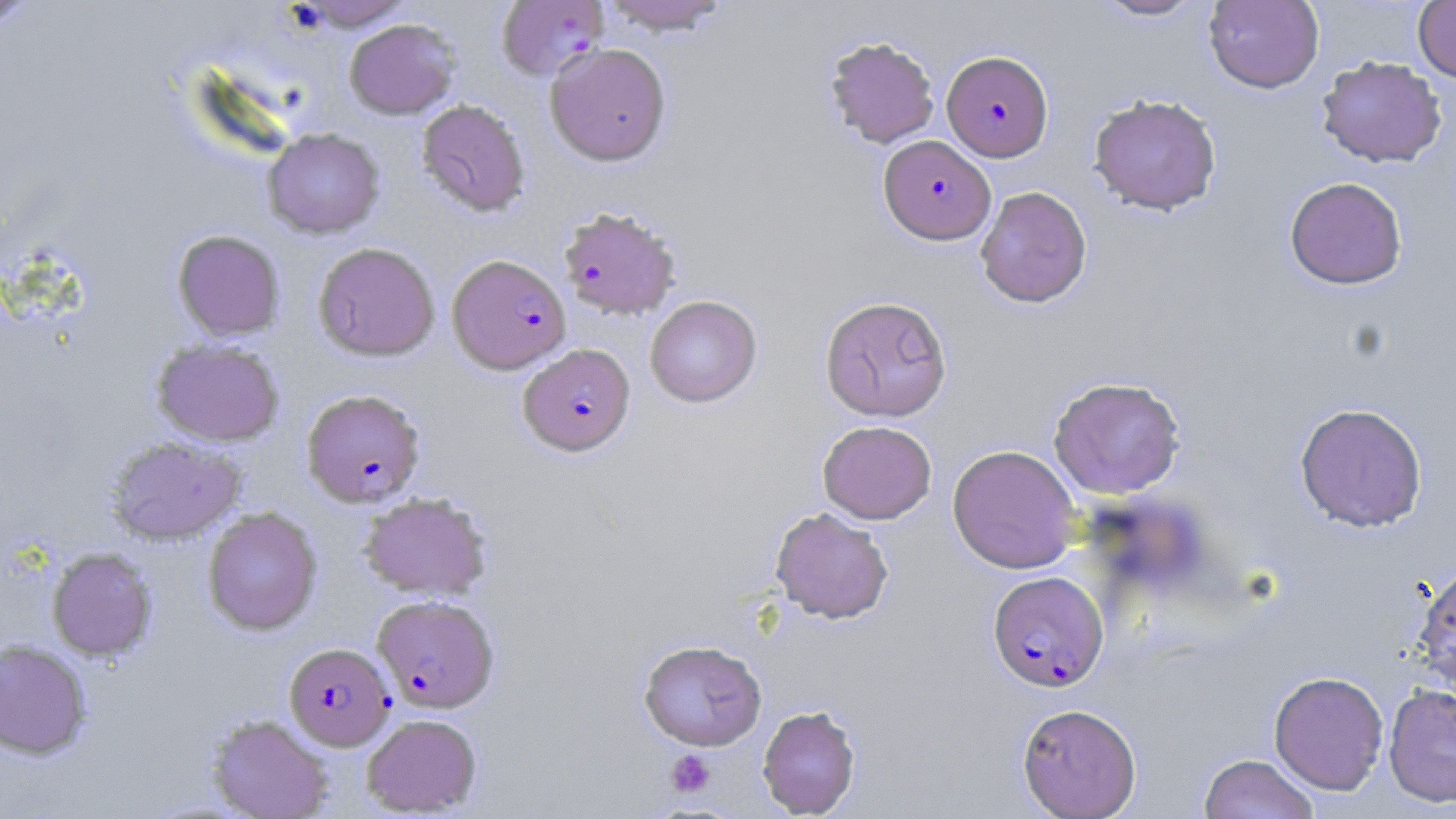

Summary:
  - Coordinate format: approximate bounding boxes as named x1/y1/x2/y2 corners in pixels
  - Uninfected red blood cell locations (subset): (x1=0, y1=0, x2=41, y2=32), (x1=292, y1=0, x2=413, y2=30), (x1=599, y1=0, x2=732, y2=35), (x1=1091, y1=0, x2=1207, y2=21), (x1=1203, y1=0, x2=1324, y2=93), (x1=1413, y1=0, x2=1456, y2=84), (x1=344, y1=18, x2=460, y2=119), (x1=824, y1=36, x2=939, y2=148), (x1=545, y1=42, x2=672, y2=166), (x1=1316, y1=56, x2=1447, y2=168), (x1=1088, y1=93, x2=1222, y2=216), (x1=416, y1=99, x2=531, y2=217), (x1=263, y1=128, x2=385, y2=239), (x1=1284, y1=176, x2=1408, y2=289), (x1=975, y1=186, x2=1092, y2=307), (x1=172, y1=230, x2=285, y2=341), (x1=313, y1=242, x2=440, y2=361), (x1=644, y1=295, x2=762, y2=407), (x1=819, y1=295, x2=952, y2=422), (x1=151, y1=337, x2=284, y2=447), (x1=1048, y1=376, x2=1186, y2=499), (x1=1294, y1=402, x2=1428, y2=532), (x1=817, y1=420, x2=937, y2=524), (x1=105, y1=436, x2=247, y2=545), (x1=947, y1=444, x2=1081, y2=574), (x1=358, y1=491, x2=493, y2=600), (x1=203, y1=506, x2=322, y2=635), (x1=770, y1=507, x2=894, y2=623), (x1=47, y1=547, x2=157, y2=661), (x1=1412, y1=560, x2=1456, y2=692), (x1=639, y1=639, x2=767, y2=750), (x1=0, y1=640, x2=92, y2=759), (x1=1269, y1=671, x2=1389, y2=794), (x1=1383, y1=683, x2=1456, y2=808), (x1=1017, y1=703, x2=1142, y2=818), (x1=757, y1=705, x2=861, y2=817), (x1=206, y1=713, x2=334, y2=819), (x1=361, y1=713, x2=482, y2=816), (x1=1199, y1=753, x2=1319, y2=819)
  - Platelet locations: (x1=665, y1=749, x2=715, y2=797)
  - Plasmodium falciparum-infected red blood cell locations (subset): (x1=942, y1=50, x2=1053, y2=162), (x1=879, y1=135, x2=995, y2=245), (x1=558, y1=205, x2=681, y2=319), (x1=447, y1=254, x2=570, y2=374), (x1=518, y1=344, x2=635, y2=456), (x1=302, y1=389, x2=425, y2=507), (x1=988, y1=570, x2=1109, y2=692), (x1=372, y1=594, x2=499, y2=713), (x1=284, y1=642, x2=395, y2=750)
  - Slide-level diagnosis: Plasmodium falciparum
  - Modality: light microscopy
  - Magnification: 1000x
  - Stain: May-Grünwald-Giemsa
  - Image size: 1456×819 pixels
  - Preparation: thin blood smear
  - Field of view: single